Classify this cell by malaria status.
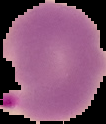

It is parasitized.

image_type: segmented cell region with the area outside set to black
preparation: thin blood film
image_size: 106×124 pixels